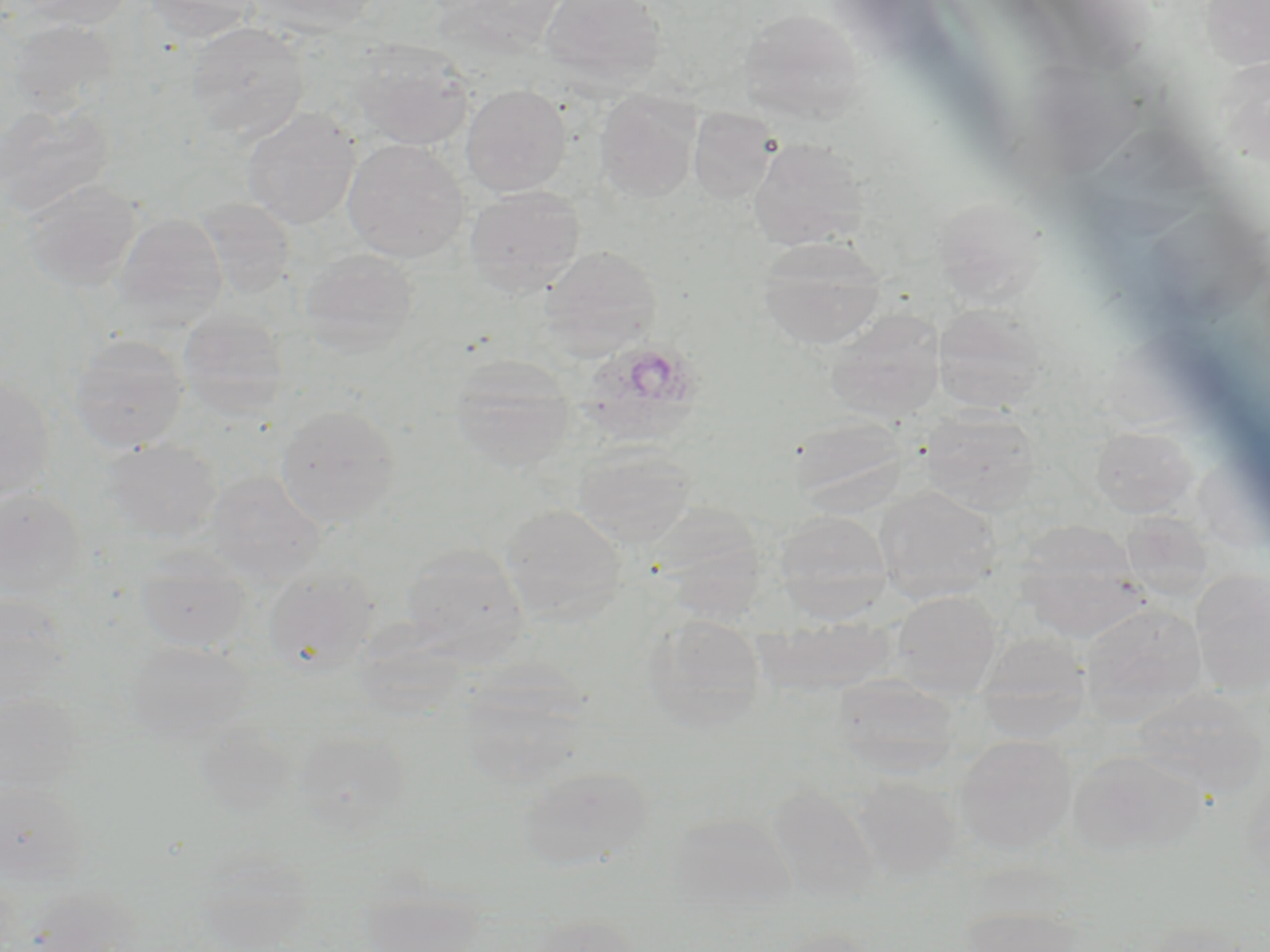
Summary:
  - Coordinate format: approximate bounding boxes as named x1/y1/x2/y2 corners in pixels
  - Plasmodium ovale-infected red blood cell locations: (x1=577, y1=341, x2=705, y2=445)
  - Uninfected red blood cell locations: (x1=19, y1=0, x2=136, y2=30), (x1=142, y1=0, x2=261, y2=43), (x1=249, y1=0, x2=381, y2=35), (x1=539, y1=0, x2=667, y2=87), (x1=1200, y1=0, x2=1270, y2=69), (x1=737, y1=8, x2=865, y2=123), (x1=7, y1=18, x2=118, y2=114), (x1=186, y1=22, x2=309, y2=140), (x1=351, y1=38, x2=475, y2=151), (x1=1214, y1=55, x2=1270, y2=166), (x1=461, y1=84, x2=572, y2=196), (x1=595, y1=91, x2=700, y2=203), (x1=0, y1=100, x2=114, y2=218), (x1=241, y1=107, x2=360, y2=229), (x1=688, y1=107, x2=779, y2=203), (x1=748, y1=138, x2=869, y2=250), (x1=343, y1=139, x2=469, y2=262), (x1=21, y1=179, x2=141, y2=292), (x1=464, y1=185, x2=586, y2=297), (x1=932, y1=195, x2=1048, y2=306), (x1=195, y1=199, x2=296, y2=300), (x1=1140, y1=201, x2=1269, y2=327), (x1=113, y1=212, x2=228, y2=328), (x1=756, y1=235, x2=885, y2=350), (x1=540, y1=246, x2=661, y2=357), (x1=299, y1=248, x2=420, y2=356), (x1=933, y1=304, x2=1047, y2=414), (x1=825, y1=309, x2=945, y2=422), (x1=178, y1=311, x2=289, y2=420), (x1=68, y1=334, x2=189, y2=453), (x1=448, y1=355, x2=575, y2=473), (x1=0, y1=375, x2=55, y2=502), (x1=276, y1=404, x2=400, y2=527), (x1=921, y1=408, x2=1042, y2=514), (x1=789, y1=413, x2=909, y2=512), (x1=1089, y1=424, x2=1198, y2=517), (x1=102, y1=437, x2=222, y2=542), (x1=573, y1=442, x2=696, y2=547), (x1=206, y1=471, x2=325, y2=586), (x1=874, y1=486, x2=1000, y2=602), (x1=0, y1=487, x2=87, y2=602), (x1=501, y1=503, x2=628, y2=624), (x1=645, y1=504, x2=769, y2=620), (x1=774, y1=510, x2=892, y2=622), (x1=1120, y1=512, x2=1213, y2=602), (x1=1013, y1=526, x2=1148, y2=640), (x1=402, y1=543, x2=530, y2=663), (x1=134, y1=550, x2=252, y2=653), (x1=264, y1=566, x2=379, y2=675), (x1=1190, y1=569, x2=1270, y2=696), (x1=891, y1=590, x2=1002, y2=697), (x1=0, y1=592, x2=71, y2=708), (x1=1079, y1=601, x2=1206, y2=723), (x1=641, y1=614, x2=768, y2=732), (x1=752, y1=616, x2=898, y2=695), (x1=974, y1=633, x2=1092, y2=742), (x1=127, y1=640, x2=251, y2=742), (x1=833, y1=674, x2=961, y2=777), (x1=457, y1=676, x2=593, y2=790), (x1=1130, y1=687, x2=1268, y2=799), (x1=0, y1=693, x2=84, y2=796), (x1=293, y1=729, x2=411, y2=834), (x1=955, y1=734, x2=1076, y2=852), (x1=1068, y1=749, x2=1205, y2=858), (x1=519, y1=765, x2=652, y2=869), (x1=852, y1=775, x2=963, y2=881), (x1=0, y1=782, x2=87, y2=886), (x1=766, y1=782, x2=882, y2=906), (x1=669, y1=812, x2=796, y2=916), (x1=194, y1=849, x2=313, y2=950), (x1=358, y1=885, x2=487, y2=951), (x1=25, y1=886, x2=141, y2=951), (x1=958, y1=904, x2=1088, y2=952), (x1=528, y1=914, x2=643, y2=952), (x1=764, y1=926, x2=882, y2=952)
  - Slide-level diagnosis: Plasmodium ovale
  - Magnification: 1000x
  - Image size: 1270×952 pixels
  - Modality: optical microscopy
  - Stain: May-Grünwald-Giemsa
  - Field of view: one of a larger specimen
  - Preparation: thin blood film